Describe the morphology of the erythrocytes.
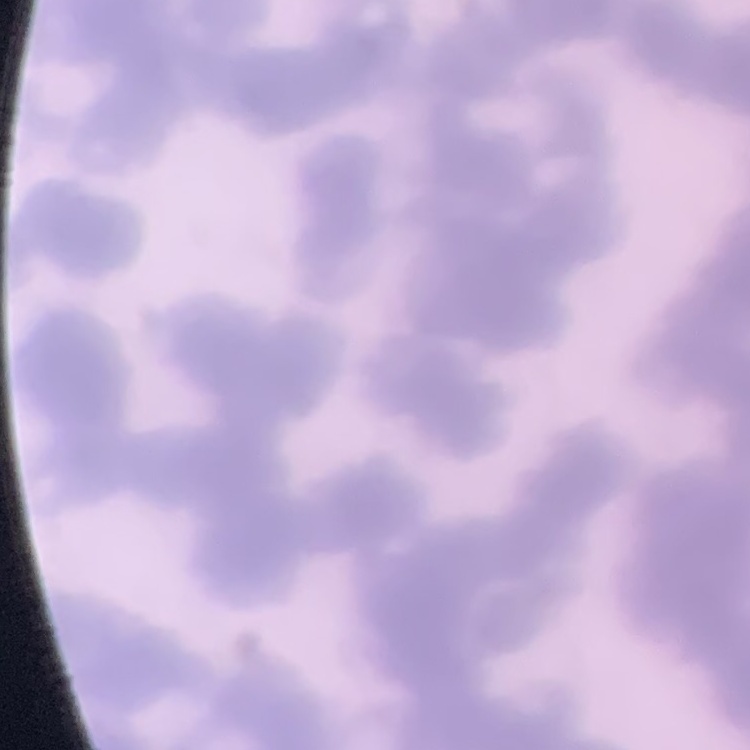

They show rouleaux formation.

preparation = thin blood film
image type = one tile cut from a larger photomicrograph
stain = Field's or Giemsa